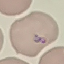
malaria status = parasitized
capture = smartphone through the microscope eyepiece
preparation = thin blood smear
image type = cell patch, automatically extracted from a larger field of view and resized to 64 × 64 pixels
stain = Giemsa